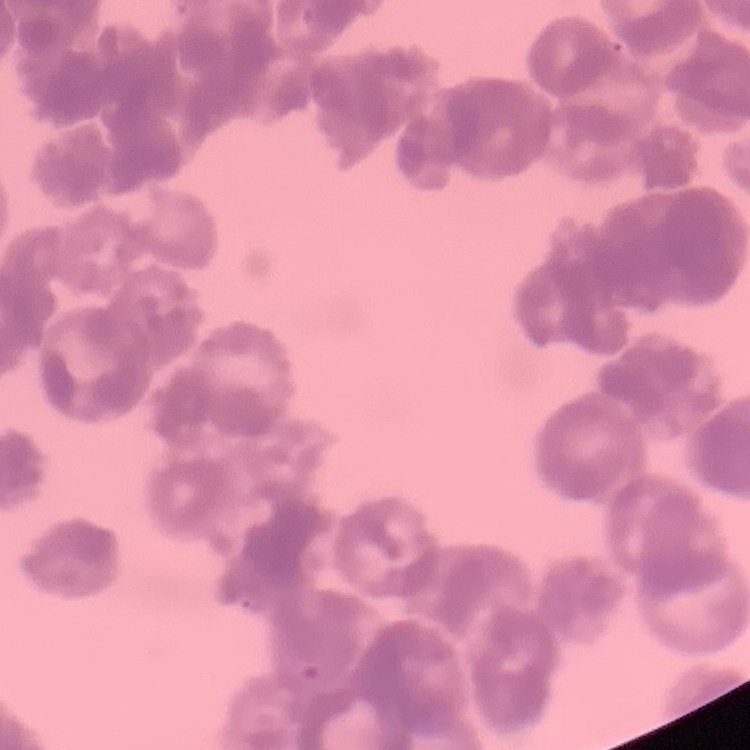 The red blood cells exhibit rouleaux formation. Stained with either Field's or Giemsa. Thin peripheral smear. One tile cut from a larger photomicrograph.